Locate Plasmodium parasites and leukocytes.
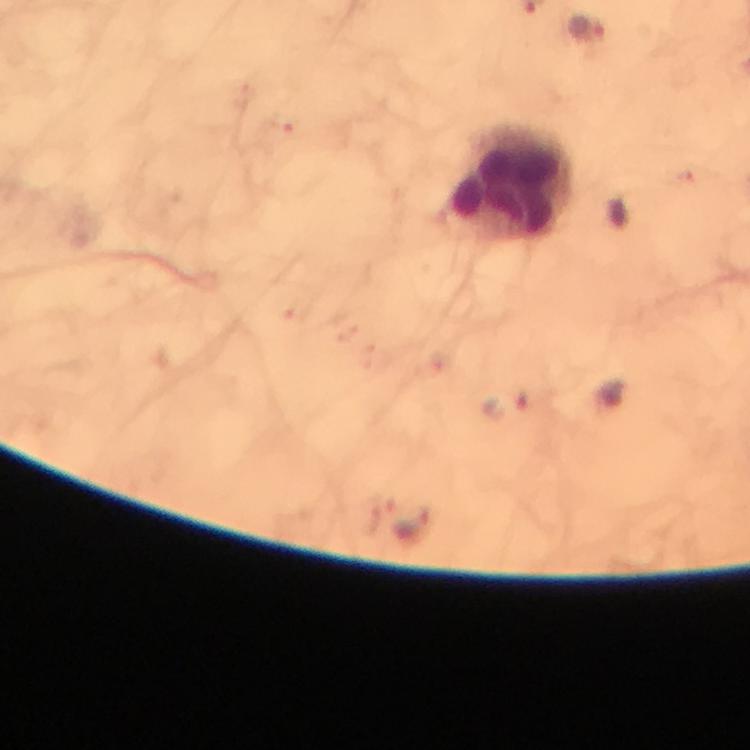
Approximate object centers, in pixels from the top-left corner.
Plasmodium parasites: (x=589, y=28), (x=508, y=406), (x=415, y=525).
Leukocytes: (x=510, y=186).

context = from a diagnostic examination for malaria
cropped from = one field of view
stain = Giemsa
preparation = thick blood smear
image size = 750×750 pixels
immersion oil = used
capture = smartphone camera through the microscope
magnification = 100x